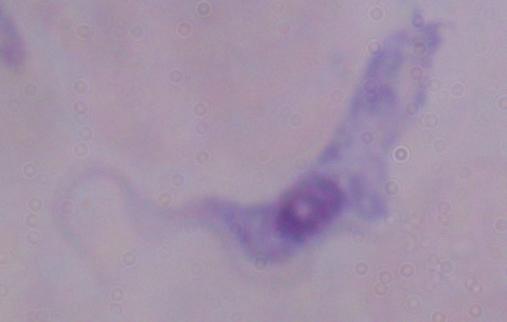

Summary:
  - Identification: trypanosome
  - Modality: micrograph
  - Magnification: 1000x